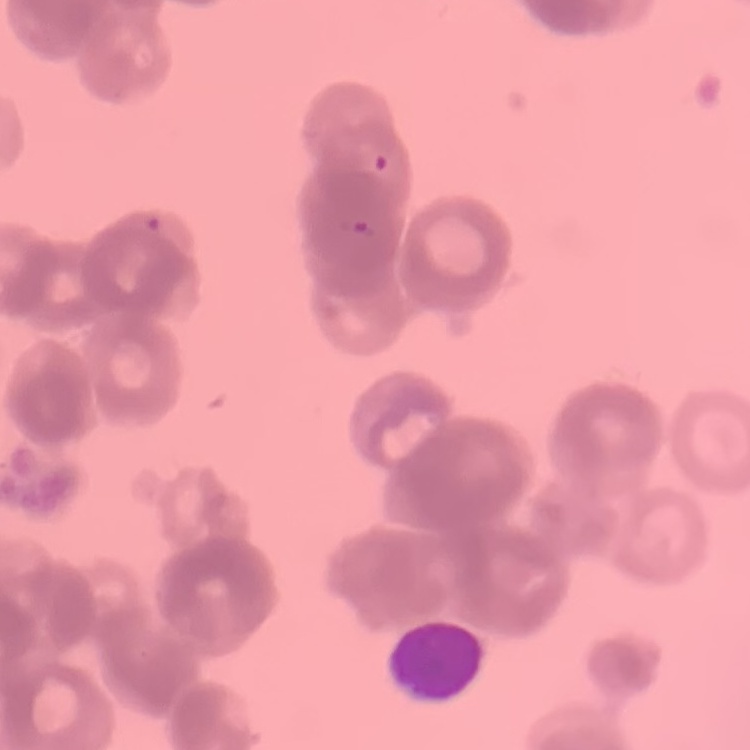
The red blood cells exhibit rouleaux formation. Thin blood smear. Square crop of a larger photomicrograph. Field's or Giemsa stain.